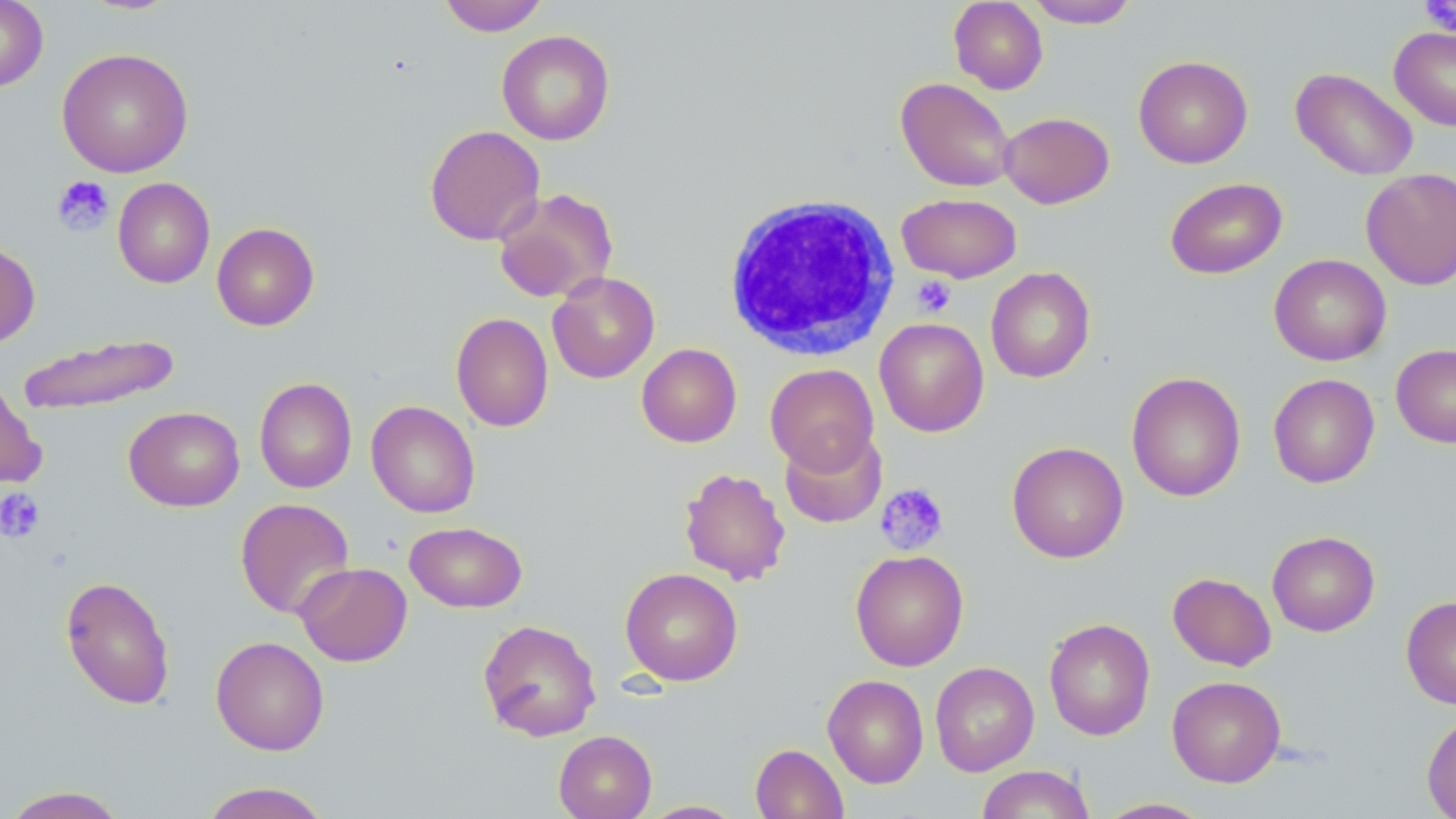
Summary:
  - Coordinate format: approximate bounding boxes as (x1,y1)-(x2,y2) corner pairs in pixels
  - Platelet locations: (1420,0)-(1456,35), (52,175)-(114,235), (911,275)-(956,318), (875,482)-(949,556), (0,487)-(45,542)
  - Uninfected red blood cell locations: (0,0)-(48,92), (438,0)-(549,36), (1026,0)-(1139,28), (949,1)-(1048,94), (1389,26)-(1456,131), (497,30)-(615,145), (57,47)-(194,177), (1133,55)-(1253,169), (1291,67)-(1418,180), (895,77)-(1016,192), (999,111)-(1115,209), (424,124)-(545,245), (1361,168)-(1456,289), (113,177)-(215,288), (1164,177)-(1287,279), (493,187)-(618,303), (897,193)-(1022,283), (211,222)-(320,331), (0,240)-(40,349), (1269,254)-(1391,366), (985,266)-(1095,383), (547,271)-(660,383), (451,312)-(554,432), (874,317)-(989,437), (16,332)-(182,416), (636,343)-(742,448), (1391,343)-(1456,448), (765,363)-(879,474), (1126,371)-(1246,502), (1268,373)-(1380,488), (254,377)-(356,493), (0,378)-(47,489), (366,400)-(481,518), (124,406)-(244,511), (780,427)-(887,529), (1006,441)-(1129,563), (678,467)-(791,586), (235,498)-(355,620), (405,521)-(527,613), (1267,531)-(1380,636), (851,550)-(969,671), (295,562)-(412,666), (620,568)-(743,686), (1168,572)-(1277,671), (59,574)-(176,710), (1401,596)-(1456,710), (1043,617)-(1156,741), (477,619)-(601,742), (210,635)-(329,756), (930,661)-(1039,776), (822,674)-(928,788), (1167,675)-(1286,787), (1421,711)-(1456,818), (553,730)-(657,819), (750,743)-(848,819), (976,765)-(1095,818), (198,782)-(332,819), (0,786)-(130,818), (1095,798)-(1213,818), (638,800)-(747,818)
  - White blood cell locations: (721,193)-(901,360)
  - Slide-level diagnosis: negative for blood parasites
  - Stain: May-Grünwald-Giemsa
  - Preparation: thin blood film
  - Modality: light microscopy
  - Image size: 1456×819 pixels
  - Field of view: one of a larger specimen
  - Magnification: 1000x